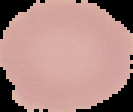
image_type: segmented cell region on a black background
image_size: 133×112 pixels
malaria_status: uninfected
preparation: thin blood smear